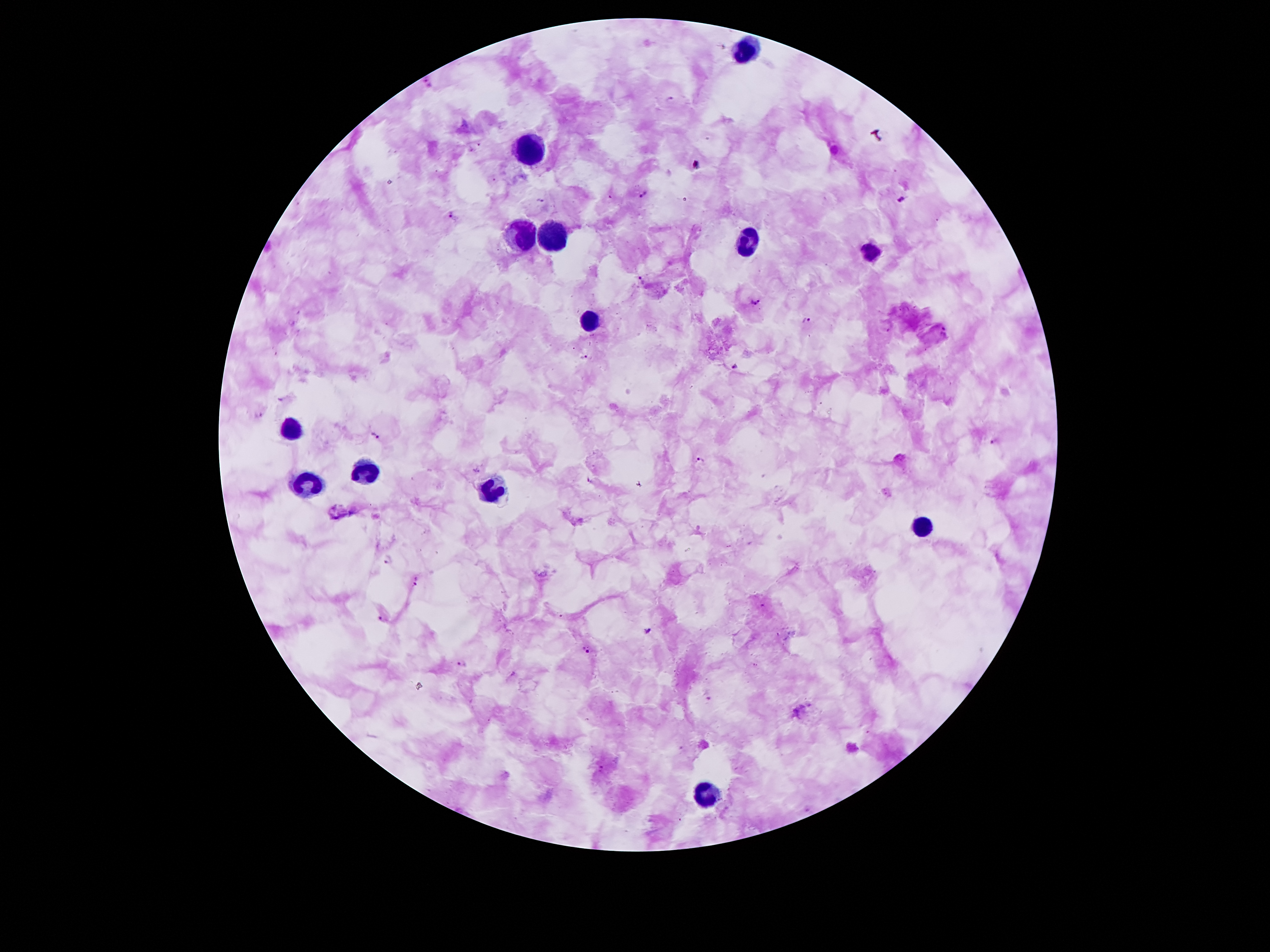

Approximate centers as {x, y} in pixels. Leukocyte locations: {746, 47}, {527, 149}, {550, 237}, {522, 238}, {750, 240}, {872, 252}, {592, 319}, {293, 426}, {368, 473}, {309, 485}, {492, 487}, {918, 529}, {711, 795}. Malaria parasite locations: {428, 80}, {642, 196}, {541, 199}, {901, 200}, {454, 215}, {641, 280}, {754, 301}, {807, 319}, {583, 355}, {735, 366}, {258, 414}, {374, 437}, {994, 442}, {701, 459}, {477, 471}, {639, 483}, {388, 559}, {416, 581}, {383, 618}, {647, 631}, {587, 649}, {461, 665}, {602, 765}. Image is 1270×952 pixels. Single field of view. Smartphone photograph taken through the microscope eyepiece. Thick blood smear. Giemsa stain. Patient malaria status: positive for Plasmodium falciparum. 100x magnification.